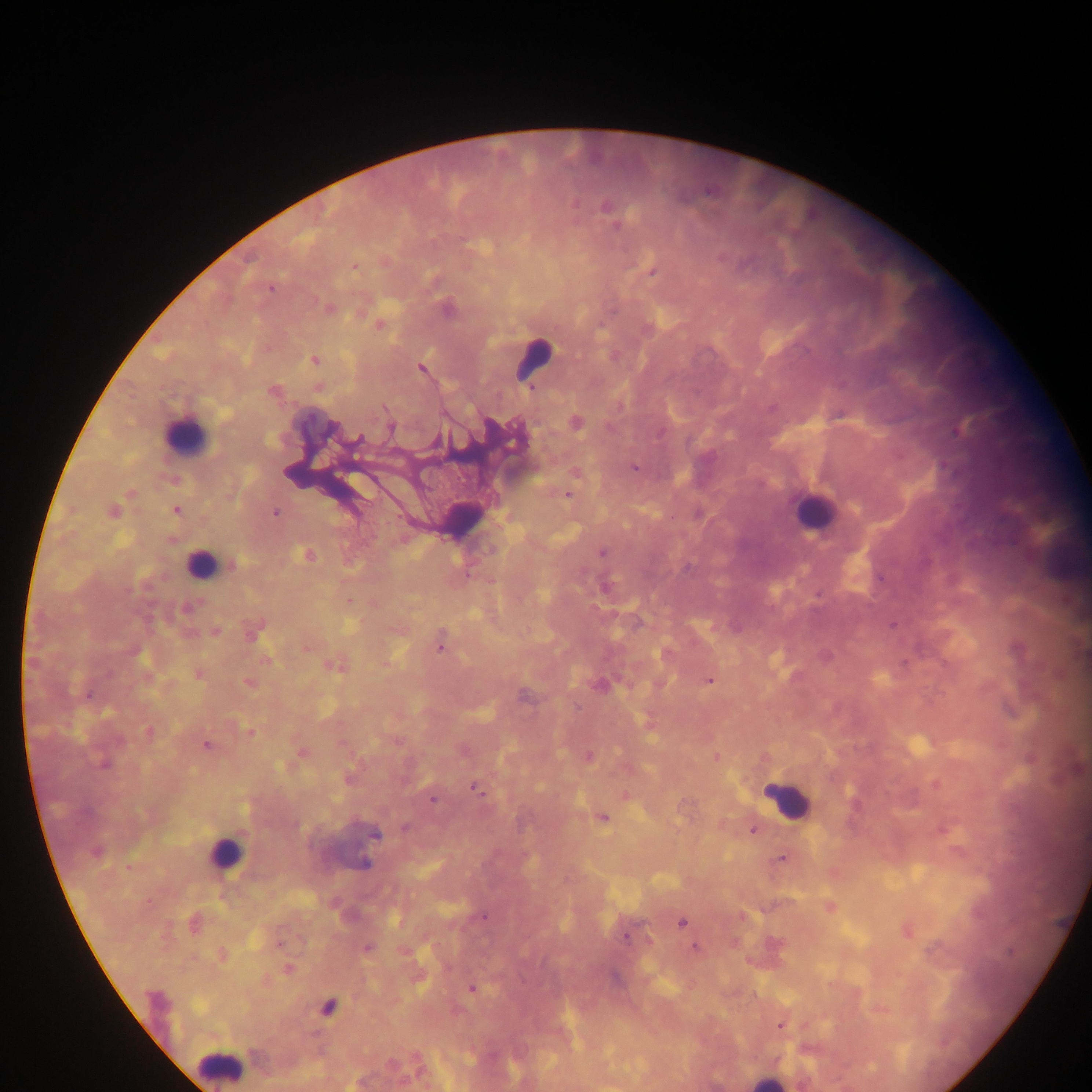 Approximate centers as (x, y) in pixels. Plasmodium parasite locations: (575, 203), (605, 206), (616, 225), (721, 255), (354, 267), (651, 272), (270, 289), (314, 298), (328, 308), (378, 324), (315, 359), (420, 366), (531, 388), (385, 408), (391, 428), (661, 433), (359, 438), (512, 442), (635, 467), (129, 494), (568, 495), (176, 510), (111, 512), (276, 513), (602, 552), (308, 554), (232, 564), (818, 594), (348, 600), (892, 624), (213, 631), (440, 646), (307, 648), (329, 665), (709, 679), (249, 682), (89, 695), (250, 732), (206, 744), (301, 752), (589, 756), (716, 757), (104, 764), (477, 791), (624, 795), (432, 800), (603, 817), (404, 828), (754, 829), (376, 835), (781, 857), (484, 916), (681, 921), (624, 936), (278, 944), (695, 947), (366, 948), (929, 951), (288, 969), (472, 988), (779, 1026). Leukocyte locations: (530, 355), (185, 439), (817, 515), (204, 563), (789, 800), (222, 859), (220, 1063). Thick blood smear. Collected in Ghana. Single field of view. Mobile-phone photograph taken through the microscope. Image is 1092×1092 pixels.